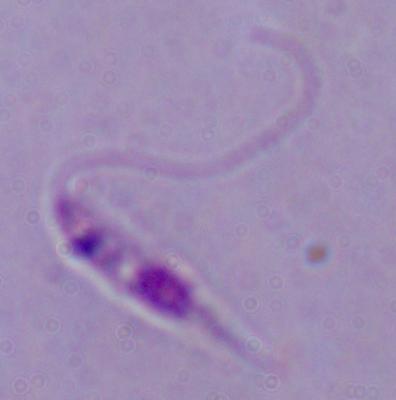

1000x magnification. Photomicrograph. A Leishmania parasite is shown.